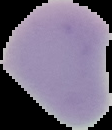
Summary:
  - Result: negative for Plasmodium parasites
  - Image type: cell region segmented out of the field of view; surrounding area masked to black
  - Preparation: thin blood film
  - Image size: 112×130 pixels